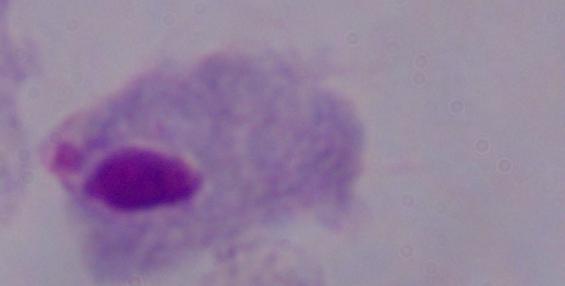

magnification: 1000x
modality: photomicrograph
identification: trichomonad